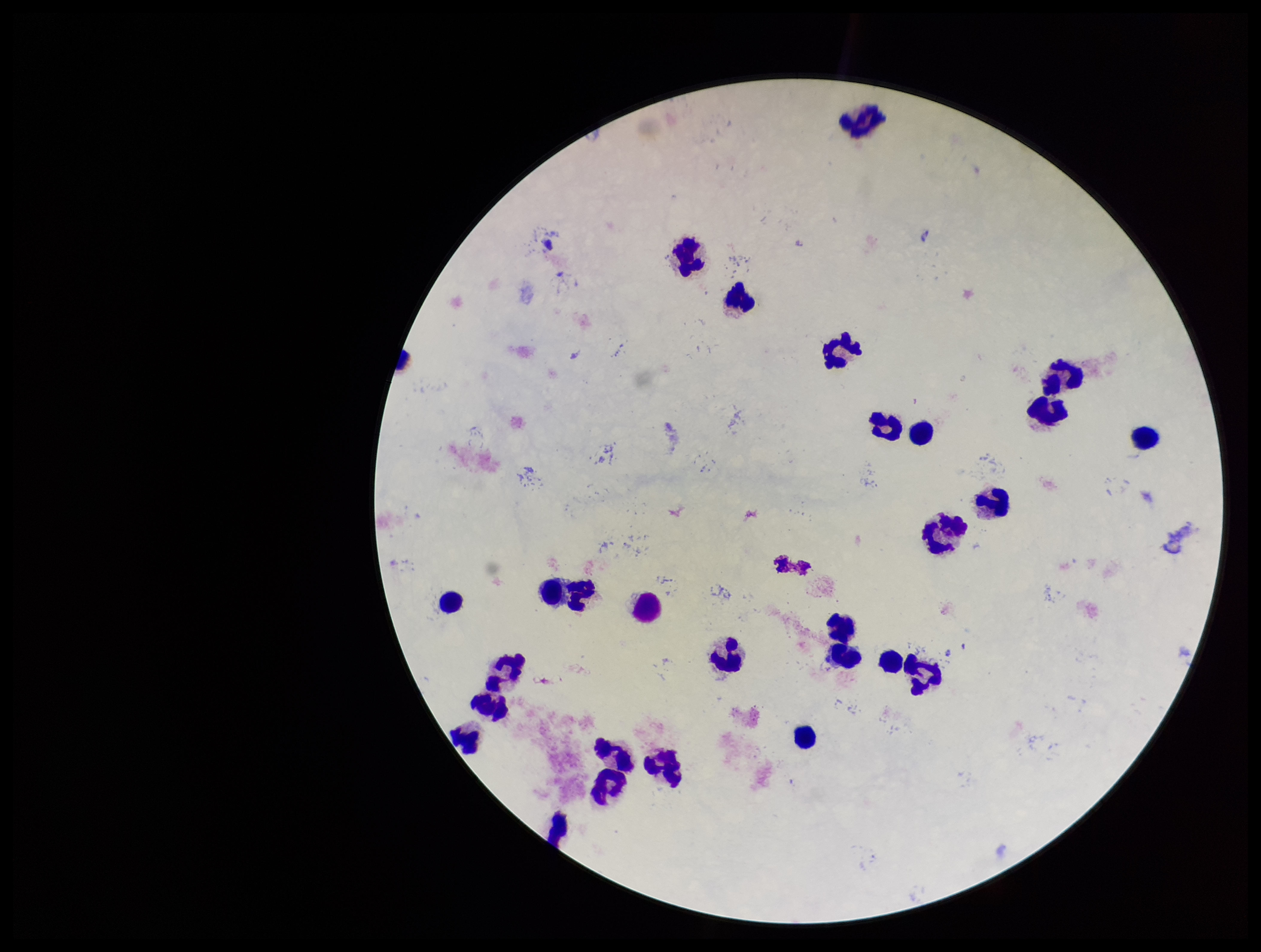

Preparation: thick. Leukocyte count: 27. Stained with Giemsa. Photographed through the microscope eyepiece with a smartphone camera. Parasite count: 0. Image is 1261×952 pixels. One field from this slide. Patient malaria status: negative. Plasmodium parasites: none detected.